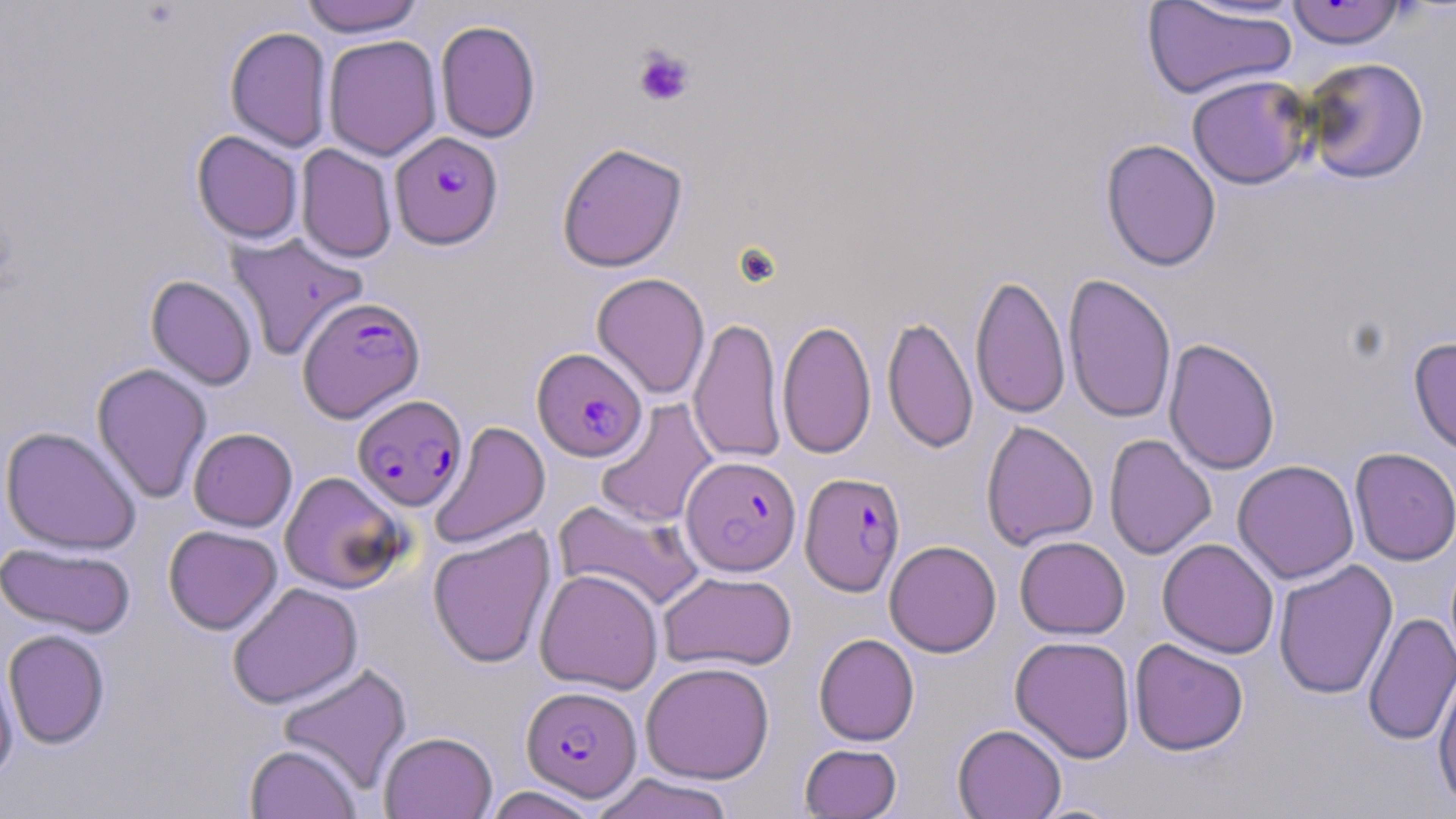
Summary:
  - Coordinate format: approximate bounding boxes as named x1/y1/x2/y2 corners in pixels
  - Plasmodium falciparum-infected red blood cell locations: (x1=390, y1=132, x2=503, y2=249), (x1=298, y1=296, x2=425, y2=422), (x1=532, y1=347, x2=647, y2=461), (x1=352, y1=394, x2=467, y2=511), (x1=681, y1=456, x2=801, y2=575), (x1=800, y1=472, x2=905, y2=597), (x1=521, y1=685, x2=642, y2=801)
  - Platelet locations: (x1=632, y1=46, x2=695, y2=108)
  - Uninfected red blood cell locations: (x1=300, y1=0, x2=425, y2=37), (x1=1142, y1=1, x2=1299, y2=101), (x1=1284, y1=1, x2=1407, y2=49), (x1=435, y1=19, x2=541, y2=143), (x1=225, y1=26, x2=333, y2=152), (x1=323, y1=35, x2=443, y2=161), (x1=1300, y1=56, x2=1431, y2=185), (x1=1186, y1=74, x2=1315, y2=190), (x1=191, y1=130, x2=304, y2=244), (x1=1101, y1=138, x2=1222, y2=271), (x1=556, y1=141, x2=688, y2=272), (x1=296, y1=144, x2=397, y2=263), (x1=226, y1=231, x2=369, y2=362), (x1=1062, y1=272, x2=1177, y2=424), (x1=591, y1=273, x2=711, y2=400), (x1=970, y1=273, x2=1071, y2=420), (x1=146, y1=275, x2=258, y2=390), (x1=882, y1=315, x2=978, y2=454), (x1=689, y1=316, x2=786, y2=465), (x1=777, y1=318, x2=876, y2=460), (x1=1408, y1=336, x2=1456, y2=458), (x1=1164, y1=338, x2=1281, y2=476), (x1=91, y1=362, x2=213, y2=504), (x1=595, y1=398, x2=719, y2=528), (x1=981, y1=420, x2=1098, y2=551), (x1=429, y1=421, x2=550, y2=550), (x1=0, y1=426, x2=142, y2=554), (x1=188, y1=427, x2=297, y2=531), (x1=1104, y1=434, x2=1216, y2=559), (x1=1350, y1=447, x2=1456, y2=566), (x1=1232, y1=459, x2=1359, y2=584), (x1=279, y1=471, x2=409, y2=594), (x1=553, y1=497, x2=704, y2=613), (x1=163, y1=525, x2=282, y2=634), (x1=428, y1=526, x2=556, y2=669), (x1=1014, y1=535, x2=1130, y2=639), (x1=1157, y1=538, x2=1279, y2=658), (x1=884, y1=539, x2=1001, y2=657), (x1=0, y1=542, x2=137, y2=637), (x1=1273, y1=559, x2=1398, y2=700), (x1=535, y1=569, x2=663, y2=694), (x1=658, y1=571, x2=797, y2=672), (x1=227, y1=582, x2=363, y2=708), (x1=1363, y1=612, x2=1456, y2=746), (x1=3, y1=629, x2=110, y2=749), (x1=814, y1=633, x2=920, y2=746), (x1=1009, y1=636, x2=1136, y2=762), (x1=1130, y1=638, x2=1249, y2=756), (x1=0, y1=658, x2=18, y2=786), (x1=641, y1=661, x2=775, y2=784), (x1=277, y1=663, x2=413, y2=795), (x1=1433, y1=668, x2=1456, y2=812), (x1=952, y1=723, x2=1067, y2=819), (x1=379, y1=731, x2=497, y2=818), (x1=244, y1=743, x2=362, y2=819), (x1=799, y1=743, x2=902, y2=818), (x1=589, y1=772, x2=736, y2=819), (x1=481, y1=786, x2=602, y2=819)
  - Slide-level diagnosis: Plasmodium falciparum
  - Preparation: thin blood film
  - Image size: 1456×819 pixels
  - Modality: optical microscopy
  - Field of view: single
  - Magnification: 1000x
  - Stain: May-Grünwald-Giemsa